Report the malaria status of this cell.
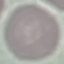

Uninfected.

Thin blood film. Giemsa stain. Photographed with a smartphone camera at the microscope eyepiece. Cell patch, automatically extracted from a larger field of view and resized to 64 × 64 pixels.